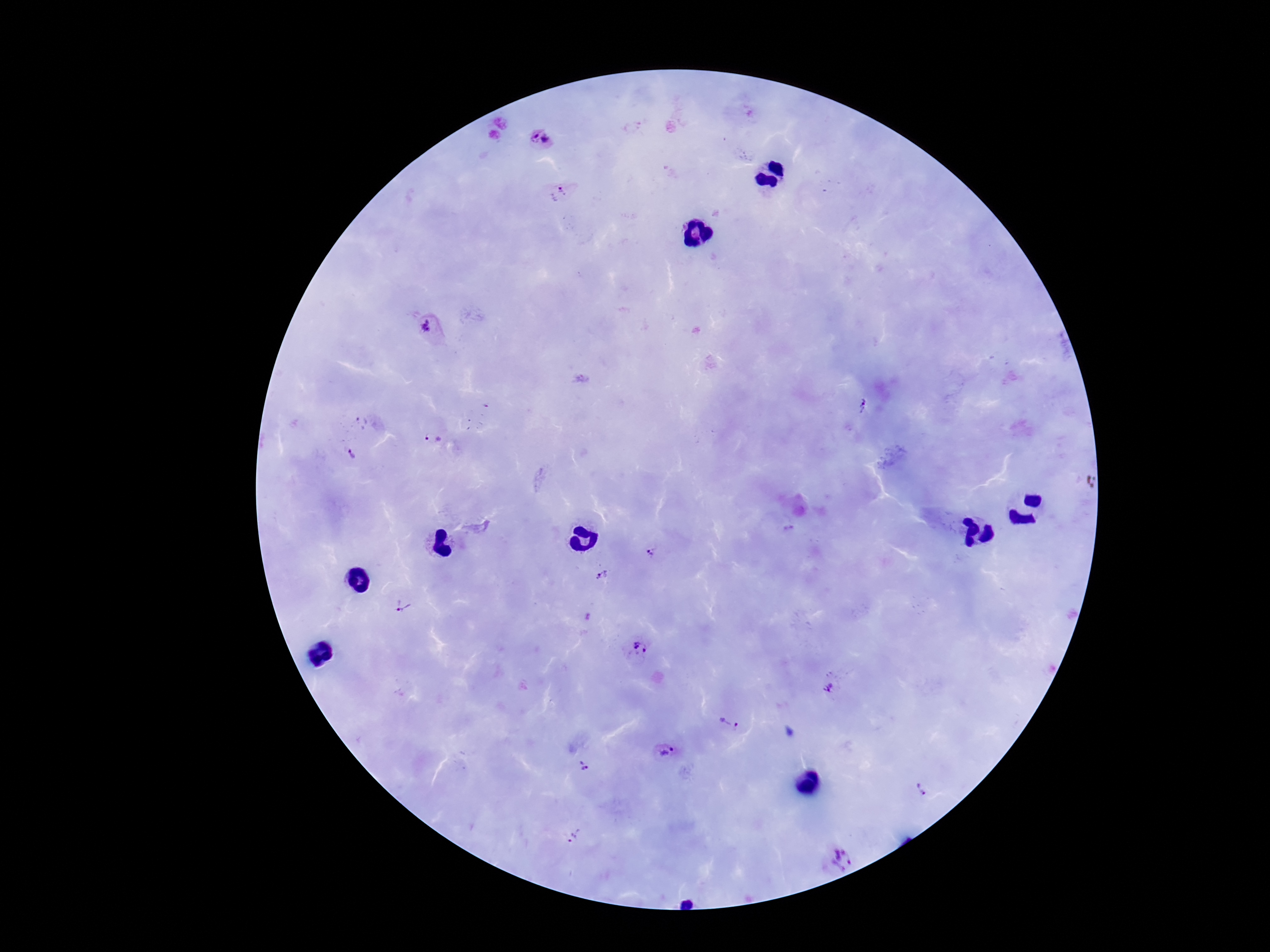
Approximate object centers, in pixels from the top-left corner.
Summary:
  - Plasmodium parasite locations: (x=541, y=139), (x=558, y=196), (x=431, y=328), (x=863, y=407), (x=358, y=422), (x=433, y=439), (x=353, y=454), (x=1085, y=481), (x=652, y=553), (x=603, y=576), (x=403, y=606), (x=638, y=645), (x=832, y=682), (x=733, y=713), (x=664, y=753), (x=588, y=766), (x=922, y=788), (x=573, y=836), (x=837, y=859)
  - Magnification: 100x
  - Patient malaria status: positive
  - Stain: Giemsa
  - Field of view: one from this slide
  - Capture: smartphone camera through the microscope eyepiece
  - Preparation: thick blood film
  - Image size: 1270×952 pixels